Assess this cell for malaria.
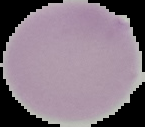
It is uninfected.

preparation: thin blood film
image_size: 145×127 pixels
image_type: cell region segmented out of the field of view; surrounding area masked to black